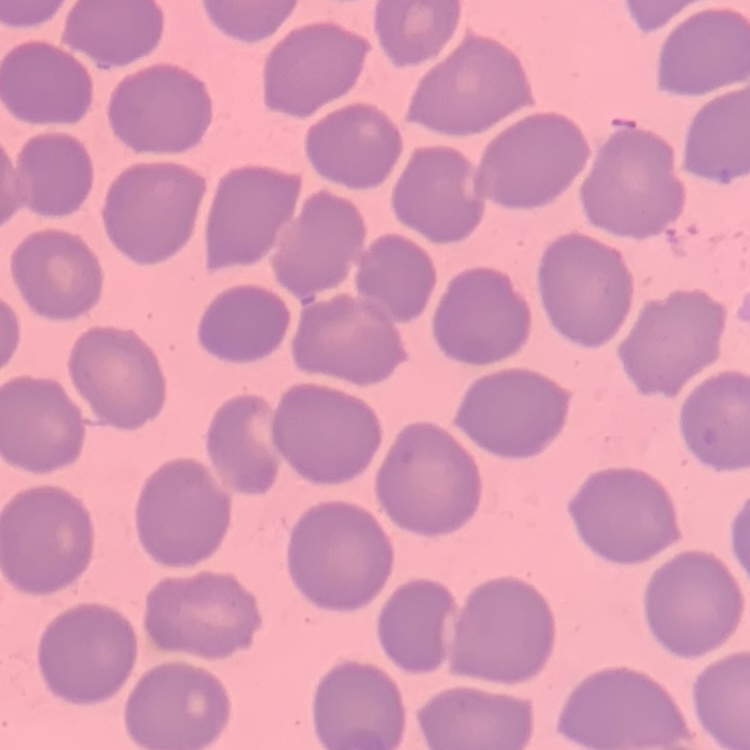

erythrocyte_morphology: no rouleaux formation
stain: Field's or Giemsa
preparation: thin peripheral smear
image_type: square crop of a larger photomicrograph